Describe the morphology of the red blood cells.
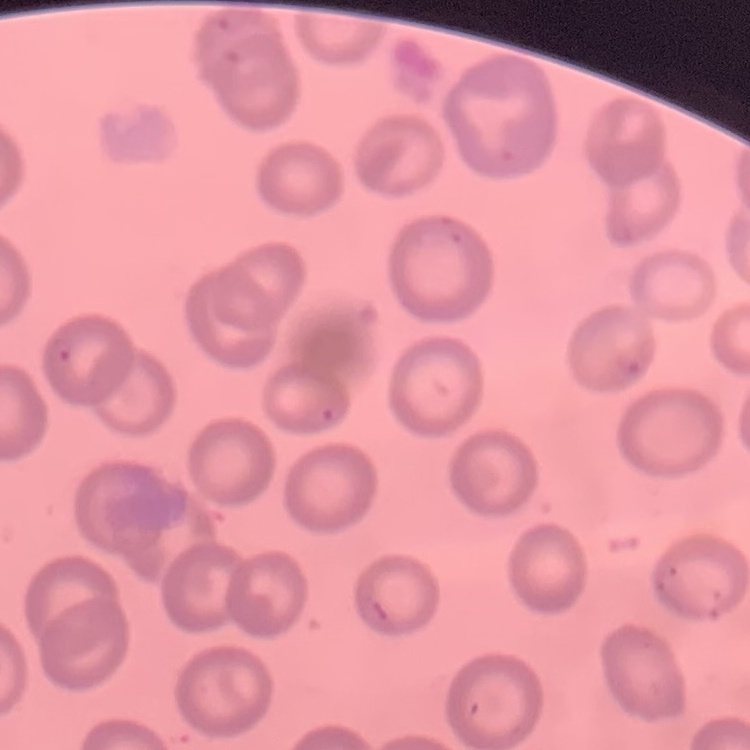

No rouleaux formation.

Thin blood smear. Square crop of a larger photomicrograph. Field's or Giemsa stain.